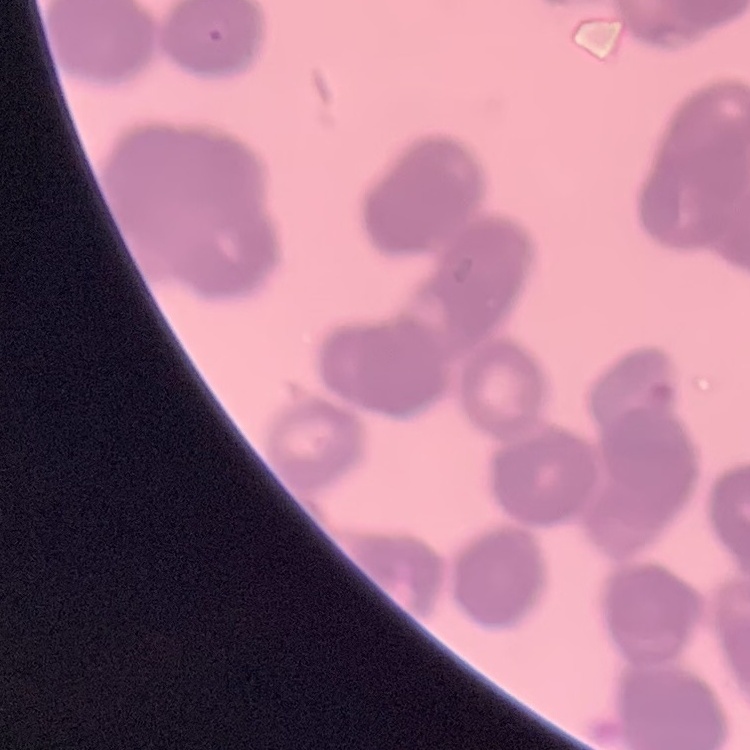

erythrocyte morphology = rouleaux formation
stain = Field's or Giemsa
image type = one tile cut from a larger photomicrograph
preparation = thin blood smear